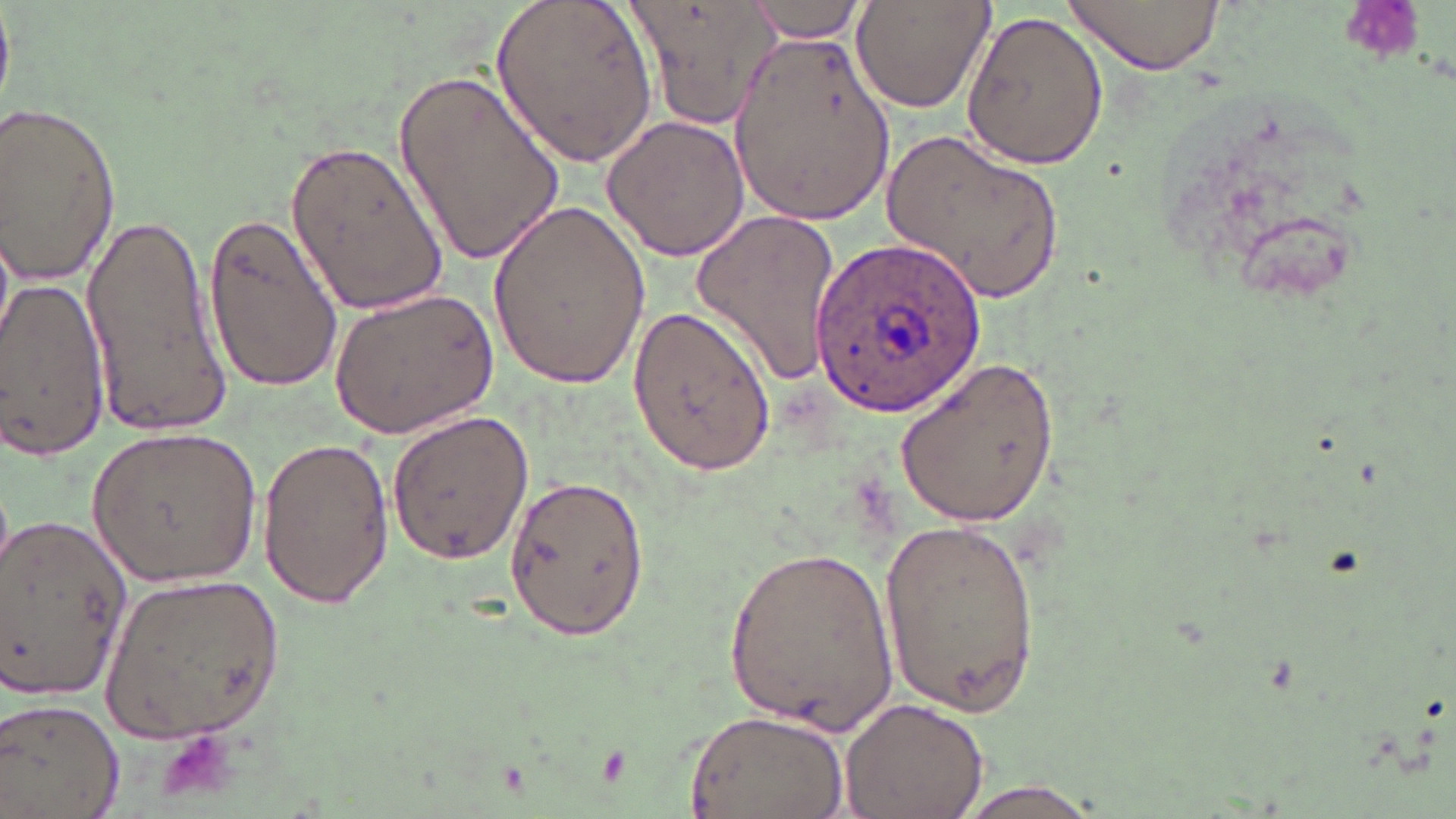
Summary:
  - Coordinate format: approximate bounding boxes as (x1,y1)-(x2,y2) corner pairs in pixels
  - Platelet locations: (156,726)-(242,804)
  - Uninfected red blood cell locations: (494,0)-(660,170), (627,0)-(778,130), (849,0)-(993,114), (1063,0)-(1225,75), (745,2)-(872,43), (0,4)-(13,115), (960,10)-(1109,172), (729,29)-(895,227), (396,66)-(567,271), (0,100)-(124,290), (601,116)-(751,260), (884,128)-(1065,303), (285,135)-(450,318), (487,196)-(652,390), (82,206)-(230,439), (690,206)-(845,391), (200,209)-(343,397), (0,279)-(110,459), (328,288)-(498,437), (626,309)-(773,477), (891,355)-(1067,527), (388,410)-(534,562), (87,426)-(266,587), (257,433)-(394,613), (506,474)-(646,637), (1,512)-(134,700), (876,513)-(1041,715), (723,540)-(897,736), (104,570)-(288,742), (0,696)-(126,819), (840,696)-(991,819), (684,710)-(848,818), (948,776)-(1111,819)
  - Plasmodium ovale-infected red blood cell locations: (814,235)-(987,415)
  - Slide-level diagnosis: Plasmodium ovale
  - Preparation: thin blood film
  - Modality: optical microscopy
  - Field of view: one of a larger specimen
  - Magnification: 1000x
  - Stain: May-Grünwald-Giemsa
  - Image size: 1456×819 pixels